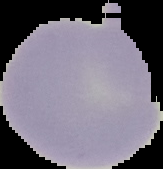
result = no malaria parasites detected
preparation = thin blood film
image size = 163×169 pixels
image type = segmented cell region with the area outside set to black